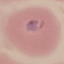
malaria status = parasitized
preparation = thin blood smear
stain = Giemsa
image type = automatically extracted cell patch, resized to 64 × 64 pixels
capture = smartphone camera at the microscope eyepiece